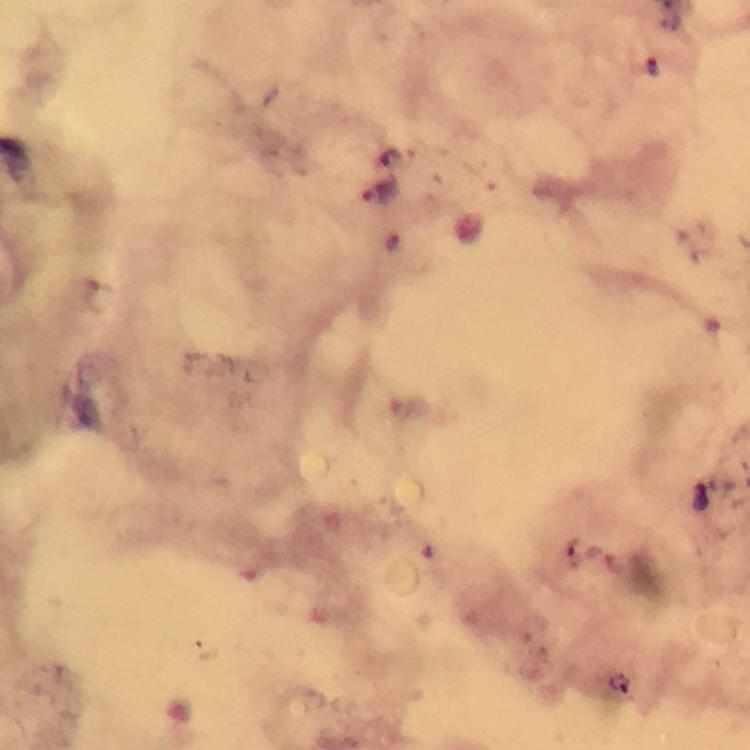

image size = 750×750 pixels
context = from a diagnostic examination for malaria
preparation = thick blood smear
capture = smartphone photograph through a microscope
cropped from = a single field of view
immersion oil = applied
Plasmodium parasite locations = approximate object centers, in pixels from the top-left corner: (x=654, y=66), (x=394, y=157), (x=382, y=193), (x=392, y=240), (x=699, y=498), (x=616, y=686)
magnification = 100x
stain = Giemsa